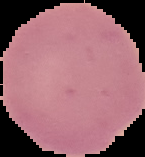

Cell region segmented out of the field of view; the surrounding area is masked to black. Malaria status: uninfected. Image is 145×157 pixels. From a thin blood smear.